Assess this cell for malaria.
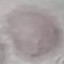

Uninfected.

Photographed with a smartphone camera at the microscope eyepiece. Thin blood smear. Automatically extracted cell patch, resized to 64 × 64 pixels. Giemsa-stained preparation.